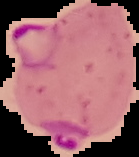

image size = 139×157 pixels
malaria status = parasitized
image type = cell region segmented out of the field of view; surrounding area masked to black
preparation = thin blood smear